Name the parasite shown.
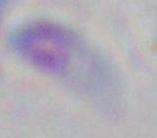
This is Toxoplasma gondii.

modality: photomicrograph
magnification: 1000x